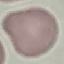

Summary:
  - Malaria status: uninfected
  - Preparation: thin blood smear
  - Stain: Giemsa
  - Image type: automatically extracted cell patch, resized to 64 × 64 pixels
  - Capture: smartphone camera at the microscope eyepiece